Assess this cell for malaria.
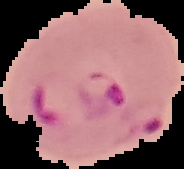

Parasitized.

Summary:
  - Preparation: thin blood smear
  - Image type: segmented cell region with the area outside set to black
  - Image size: 184×169 pixels